Give the position of every leukocyte visible.
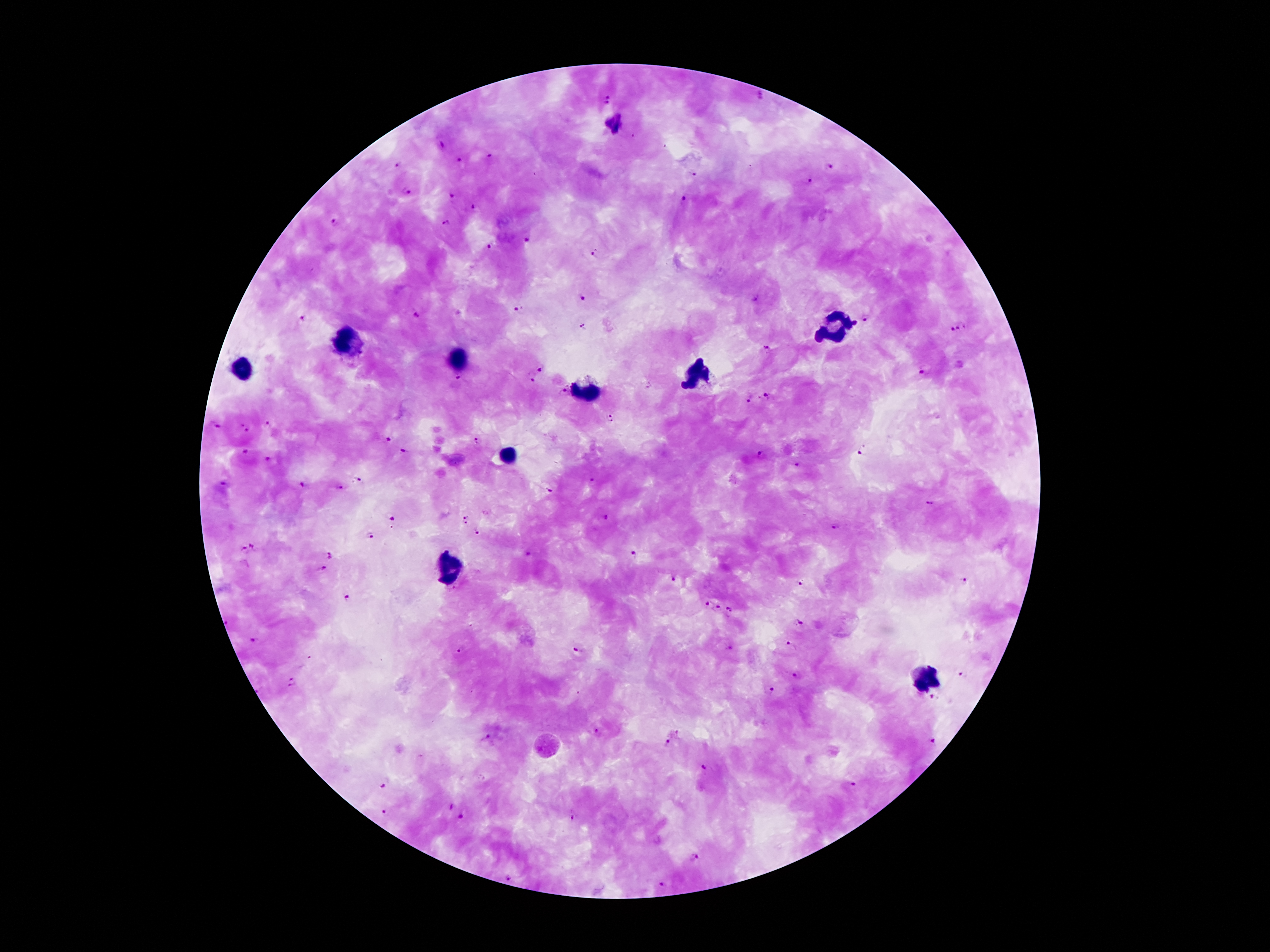
Approximate object centers, in pixels from the top-left corner.
Leukocytes: (x=834, y=327), (x=343, y=341), (x=456, y=357), (x=241, y=369), (x=699, y=377), (x=589, y=391), (x=506, y=454), (x=450, y=566), (x=922, y=682).

Summary:
  - Malaria parasite locations: (x=759, y=95), (x=607, y=99), (x=441, y=146), (x=490, y=158), (x=462, y=161), (x=399, y=164), (x=831, y=167), (x=693, y=174), (x=806, y=181), (x=406, y=191), (x=452, y=196), (x=683, y=199), (x=474, y=209), (x=335, y=221), (x=446, y=224), (x=527, y=240), (x=490, y=247), (x=594, y=254), (x=581, y=298), (x=520, y=309), (x=417, y=314), (x=303, y=318), (x=864, y=319), (x=583, y=327), (x=961, y=328), (x=952, y=330), (x=765, y=347), (x=542, y=368), (x=924, y=372), (x=457, y=379), (x=533, y=379), (x=562, y=391), (x=765, y=395), (x=748, y=400), (x=610, y=418), (x=267, y=423), (x=217, y=426), (x=244, y=427), (x=387, y=438), (x=477, y=441), (x=402, y=451), (x=864, y=451), (x=244, y=452), (x=760, y=453), (x=268, y=460), (x=797, y=465), (x=359, y=478), (x=593, y=480), (x=223, y=484), (x=301, y=485), (x=338, y=488), (x=548, y=490), (x=929, y=504), (x=392, y=517), (x=606, y=517), (x=465, y=520), (x=835, y=528), (x=476, y=531), (x=368, y=536), (x=253, y=544), (x=244, y=550), (x=331, y=555), (x=634, y=555), (x=323, y=569), (x=672, y=579), (x=963, y=580), (x=802, y=584), (x=453, y=589), (x=347, y=597), (x=706, y=602), (x=718, y=608), (x=731, y=609), (x=800, y=623), (x=254, y=640), (x=789, y=647), (x=729, y=649), (x=461, y=651), (x=579, y=651), (x=794, y=675), (x=966, y=675), (x=290, y=682), (x=770, y=689), (x=933, y=698), (x=597, y=731), (x=488, y=737), (x=932, y=740), (x=667, y=742), (x=705, y=769), (x=849, y=785), (x=384, y=786), (x=451, y=806), (x=382, y=812), (x=460, y=818), (x=573, y=819), (x=697, y=856), (x=510, y=877), (x=661, y=884)
  - Stain: Giemsa
  - Patient malaria status: infected with Plasmodium falciparum
  - Image size: 1270×952 pixels
  - Field of view: one from this slide
  - Capture: smartphone through the microscope eyepiece
  - Magnification: 100x
  - Preparation: thick blood smear